Look for Plasmodium parasites.
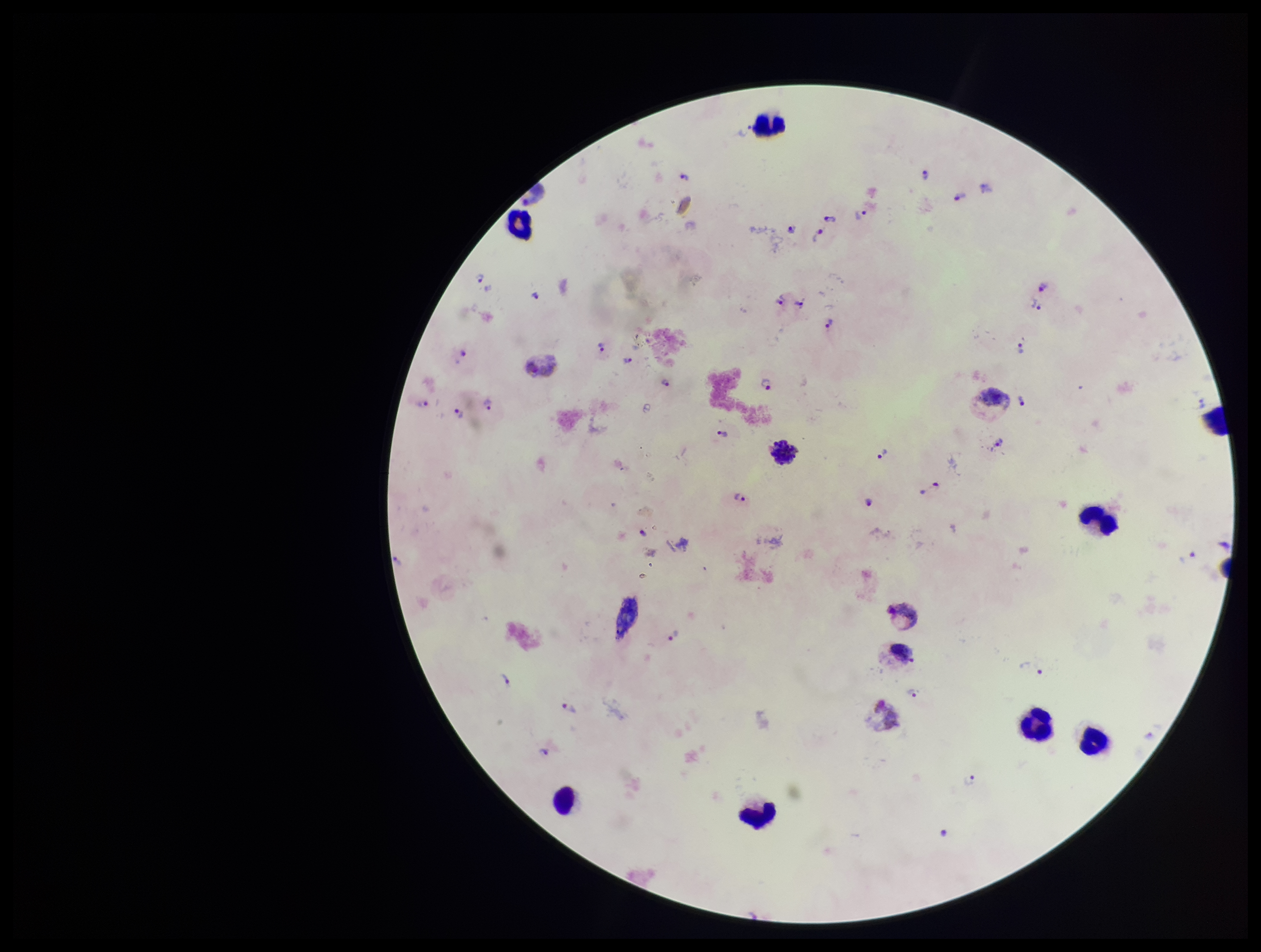

Seen.

Summary:
  - Parasite count: 37
  - Patient malaria status: infected
  - Capture: smartphone photograph through the microscope eyepiece
  - Leukocyte count: 9
  - Stain: Giemsa
  - Image size: 1261×952 pixels
  - Preparation: thick smear
  - Species reported for this patient: Plasmodium vivax
  - Field of view: single